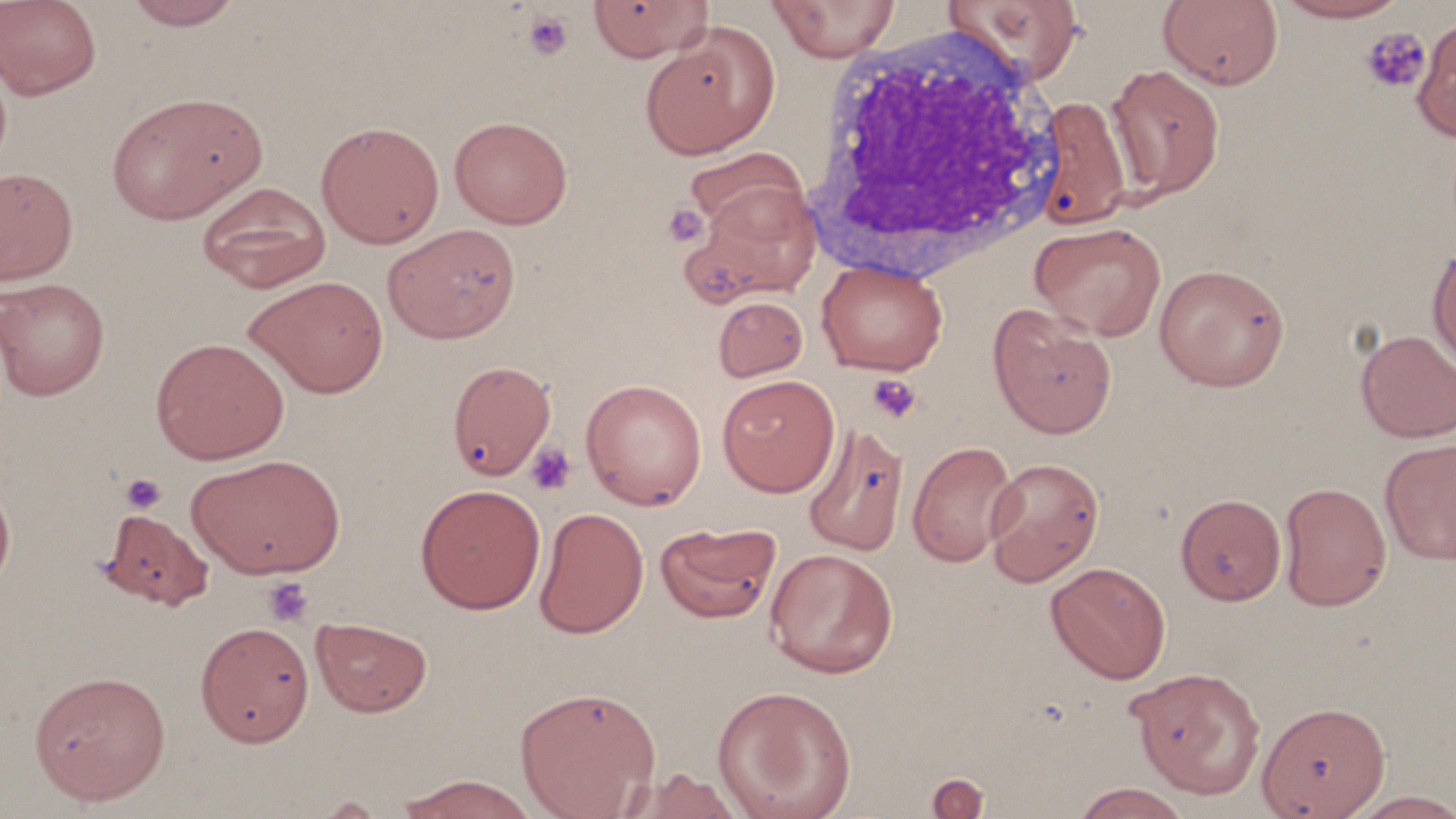 Approximate bounding boxes as (x1,y1)-(x2,y2) corner pairs in pixels. Platelet locations: (522,10)-(574,60), (1360,26)-(1431,95), (661,202)-(709,247), (867,374)-(922,423), (524,442)-(577,496), (119,473)-(167,514), (262,576)-(315,627). White blood cell locations: (798,18)-(1071,290). Uninfected red blood cell locations: (0,0)-(102,100), (121,0)-(246,30), (945,0)-(1086,85), (1158,0)-(1284,90), (1271,0)-(1411,23), (587,1)-(712,62), (766,1)-(901,61), (1412,19)-(1456,142), (640,26)-(778,159), (1105,64)-(1225,200), (106,91)-(266,224), (1032,95)-(1132,230), (449,115)-(573,229), (316,120)-(445,249), (683,147)-(809,240), (0,166)-(78,286), (195,182)-(332,293), (686,184)-(821,301), (1029,221)-(1166,341), (384,224)-(521,343), (1427,242)-(1456,372), (816,258)-(948,375), (1154,262)-(1290,391), (243,275)-(389,398), (0,278)-(110,401), (713,295)-(808,381), (987,304)-(1118,440), (1355,329)-(1456,442), (150,336)-(290,464), (447,359)-(556,480), (717,374)-(840,497), (580,378)-(707,510), (802,421)-(910,557), (1379,438)-(1456,564), (907,440)-(1019,567), (186,453)-(346,579), (983,457)-(1104,586), (0,476)-(16,597), (1279,481)-(1392,612), (414,483)-(546,614), (1176,493)-(1286,605), (97,506)-(214,610), (533,507)-(649,639), (655,522)-(781,623), (764,547)-(899,678), (1045,562)-(1171,684), (311,615)-(433,717), (195,621)-(314,746), (1127,666)-(1266,798), (29,669)-(171,805), (514,685)-(661,819), (712,685)-(858,819), (1256,716)-(1389,818), (619,767)-(746,819), (926,772)-(991,818), (394,774)-(539,819), (1071,782)-(1192,819), (1346,790)-(1456,818). Slide-level diagnosis: negative for blood parasites. Thin blood smear. May-Grünwald-Giemsa-stained preparation. 1000x magnification. Image is 1456×819 pixels. One field of a larger specimen. Optical microscopy.